Name the cell type shown.
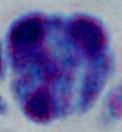
This is a leukocyte.

magnification: 1000x
modality: photomicrograph